Report the malaria status of this cell.
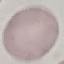

It is uninfected.

Giemsa stain. Thin blood smear. Cell patch, automatically extracted from a larger field of view and resized to 64 × 64 pixels. Photographed with a smartphone camera at the microscope eyepiece.